Locate every blood parasite and identify its species.
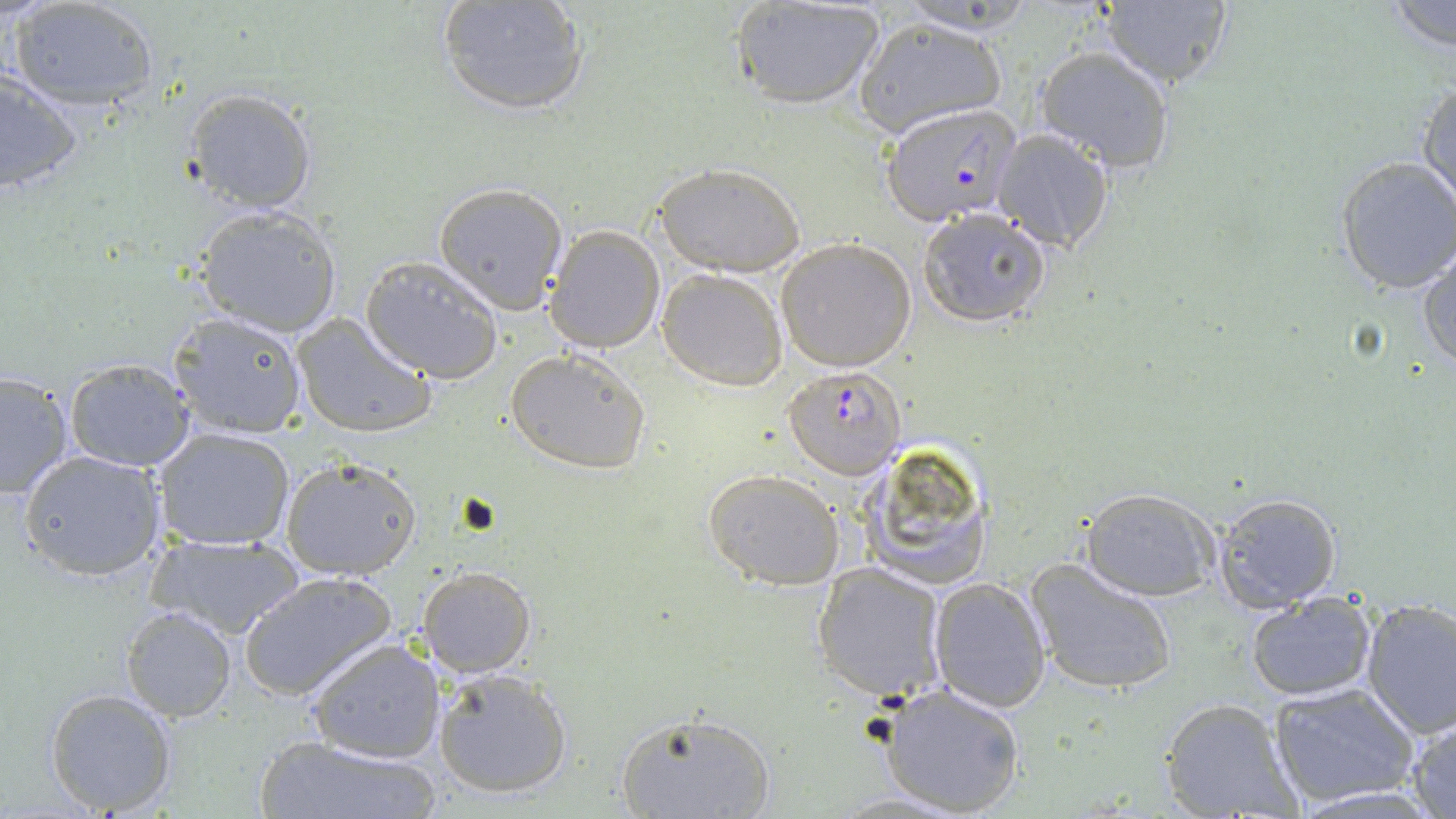

Approximate bounding boxes as (x1,y1)-(x2,y2) corner pairs in pixels.
Plasmodium falciparum-infected red blood cells: (880,103)-(1022,227), (781,366)-(906,479).
No Plasmodium ovale, Plasmodium malariae, Plasmodium vivax, Babesia divergens, or Trypanosoma brucei observed.

Summary:
  - Platelet locations: (456,494)-(502,536)
  - Uninfected red blood cell locations: (436,0)-(590,116), (894,0)-(1041,34), (9,1)-(159,114), (731,1)-(887,112), (1385,1)-(1456,52), (1094,2)-(1236,88), (850,16)-(1007,137), (1033,46)-(1177,172), (0,69)-(82,198), (1416,80)-(1456,213), (180,86)-(319,214), (992,128)-(1115,252), (1334,155)-(1456,295), (654,161)-(806,277), (432,181)-(570,315), (193,206)-(343,339), (918,206)-(1052,329), (544,224)-(667,353), (776,238)-(918,372), (1416,246)-(1456,373), (360,255)-(505,382), (658,269)-(789,391), (167,310)-(308,438), (292,311)-(433,439), (505,348)-(650,474), (62,358)-(196,472), (0,369)-(74,498), (154,427)-(298,551), (859,441)-(994,588), (17,449)-(168,581), (280,457)-(420,580), (702,468)-(845,589), (1080,487)-(1222,600), (1209,490)-(1344,610), (146,532)-(305,639), (1026,558)-(1178,696), (813,564)-(947,704), (416,565)-(537,677), (239,570)-(396,701), (928,575)-(1051,712), (1246,593)-(1376,703), (1359,598)-(1456,739), (119,606)-(235,719), (305,636)-(446,763), (430,667)-(574,799), (1268,682)-(1420,807), (878,683)-(1027,817), (45,687)-(178,816), (1159,697)-(1304,819), (614,707)-(776,818), (1405,714)-(1456,817), (254,735)-(440,819)
  - Slide-level diagnosis: Plasmodium falciparum
  - Field of view: single
  - Stain: May-Grünwald-Giemsa
  - Preparation: thin blood film
  - Modality: optical microscopy
  - Magnification: 1000x
  - Image size: 1456×819 pixels